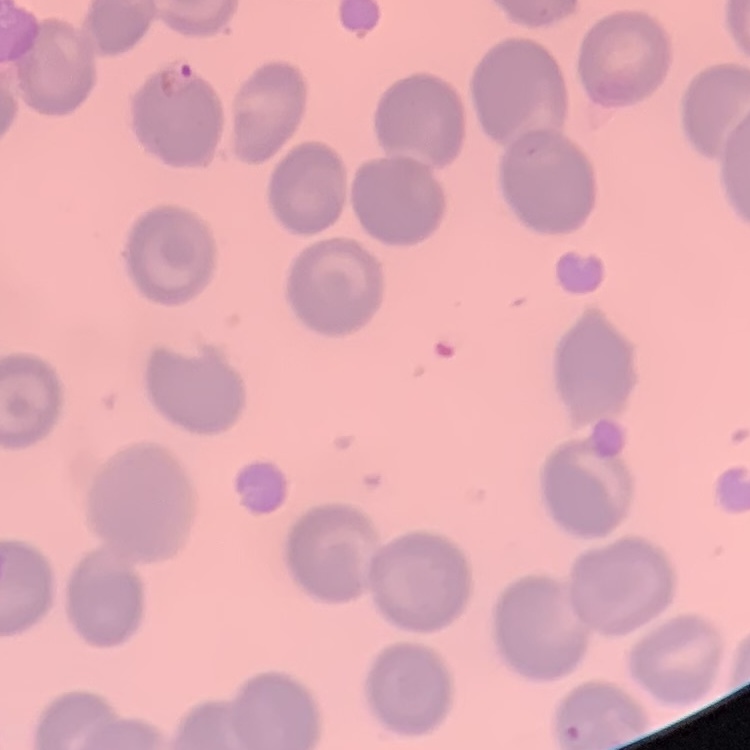
red blood cell morphology = no rouleaux formation
preparation = thin peripheral smear
image type = one tile cut from a larger photomicrograph
stain = Field's or Giemsa